Describe the morphology of the red blood cells.
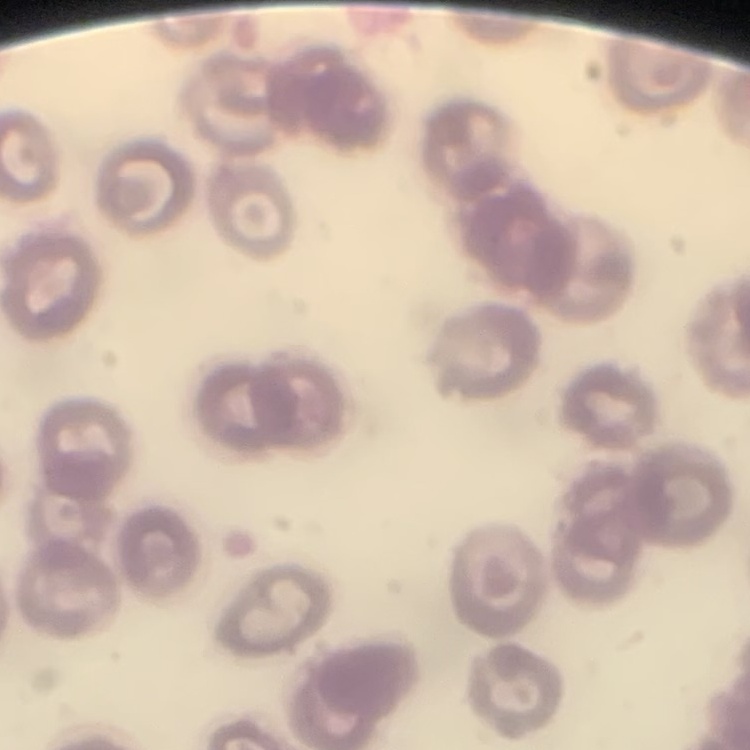
They show no rouleaux formation.

stain: Field's or Giemsa
image_type: one tile cut from a larger photomicrograph
preparation: thin peripheral smear